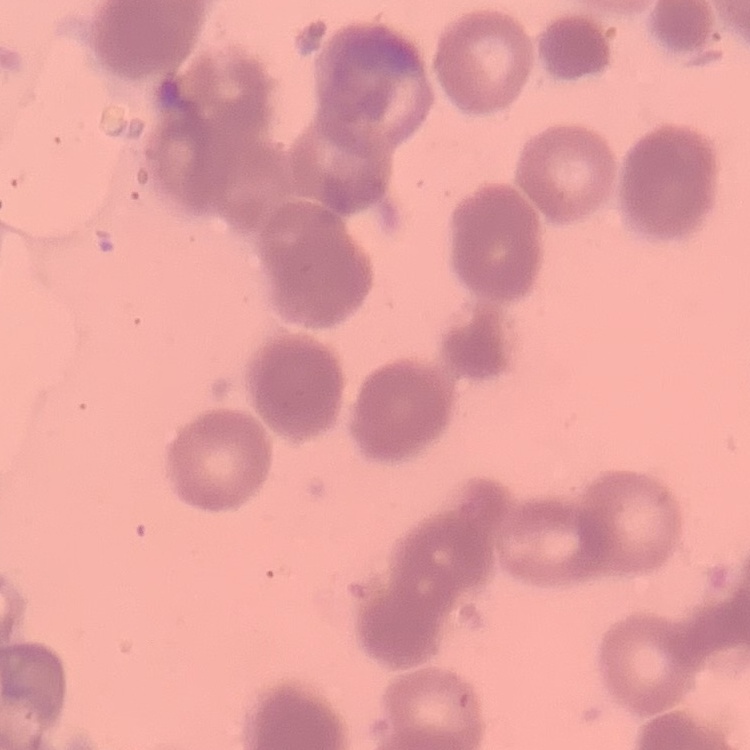
The red blood cells show rouleaux formation. Thin blood smear. Field's or Giemsa stain. Square crop of a larger photomicrograph.